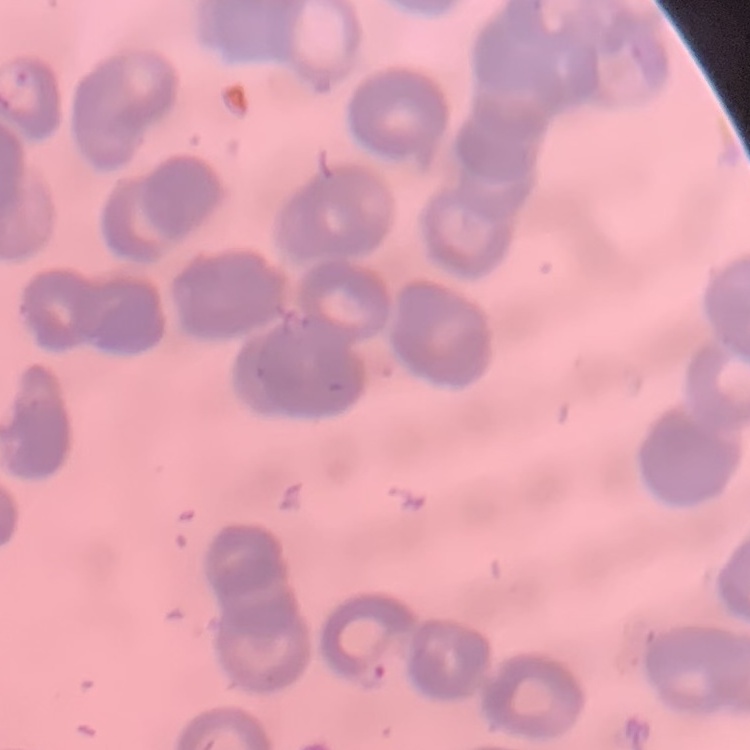

Summary:
  - Erythrocyte morphology: rouleaux formation
  - Image type: one tile cut from a larger photomicrograph
  - Preparation: thin blood film
  - Stain: Field's or Giemsa